Report the malaria status of this cell.
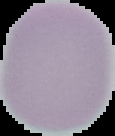

It is uninfected.

Summary:
  - Image size: 115×136 pixels
  - Image type: segmented cell region on a black background
  - Preparation: thin blood film